Classify this cell by malaria status.
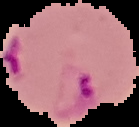

Parasitized.

From a thin blood film. The area outside the segmented cell region is set to black. Image is 139×127 pixels.